Assess this cell for malaria.
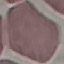

Uninfected.

Photographed with a smartphone camera at the microscope eyepiece. Automatically extracted cell patch, resized to 64 × 64 pixels. Giemsa stain. Thin smear of blood.